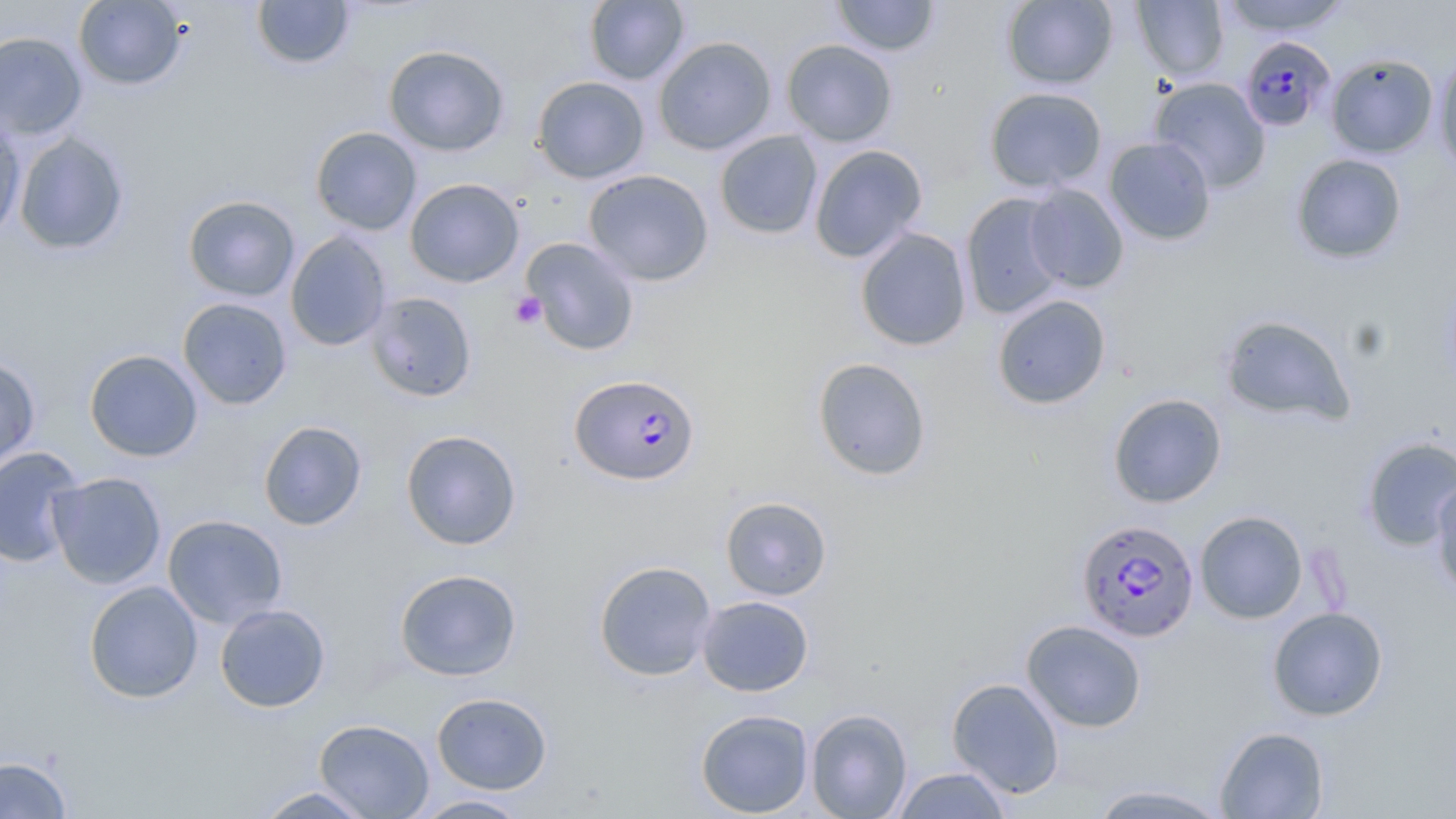

Summary:
  - Coordinate format: approximate bounding boxes as (x1, y1, x2, y2) in pixels
  - Uninfected red blood cell locations: (73, 0, 186, 91), (251, 0, 355, 70), (584, 0, 690, 86), (831, 0, 940, 57), (1000, 0, 1118, 90), (1132, 0, 1229, 81), (1219, 0, 1351, 36), (0, 31, 87, 140), (653, 36, 777, 155), (781, 39, 898, 147), (383, 44, 510, 156), (1326, 53, 1439, 158), (1433, 54, 1456, 179), (531, 76, 649, 184), (1148, 77, 1271, 193), (983, 87, 1107, 193), (0, 112, 26, 244), (310, 126, 422, 235), (715, 130, 823, 239), (13, 132, 130, 256), (1104, 137, 1216, 246), (809, 144, 927, 263), (1290, 153, 1407, 264), (583, 169, 714, 286), (405, 178, 524, 287), (1024, 184, 1130, 293), (959, 192, 1070, 320), (183, 194, 300, 302), (855, 227, 973, 352), (285, 231, 392, 351), (521, 237, 640, 356), (1440, 269, 1456, 397), (366, 292, 477, 402), (992, 294, 1111, 410), (177, 297, 293, 410), (1219, 313, 1356, 427), (84, 349, 203, 462), (0, 356, 41, 471), (812, 357, 932, 480), (1108, 393, 1227, 508), (258, 420, 368, 531), (400, 430, 522, 550), (1360, 435, 1456, 551), (0, 446, 85, 567), (48, 471, 166, 589), (1430, 476, 1456, 602), (720, 496, 832, 600), (1194, 509, 1308, 624), (163, 514, 288, 629), (593, 560, 718, 681), (394, 568, 522, 681), (84, 580, 204, 704), (697, 595, 814, 697), (214, 603, 331, 712), (1267, 606, 1388, 721), (1021, 619, 1147, 732), (946, 677, 1065, 797), (431, 691, 552, 794), (805, 708, 913, 819), (695, 709, 814, 817), (314, 718, 434, 818), (1214, 725, 1329, 818), (0, 756, 72, 818), (891, 766, 1013, 818), (1086, 783, 1235, 818), (252, 786, 378, 818), (411, 794, 533, 818)
  - Platelet locations: (510, 292, 546, 329)
  - Plasmodium falciparum-infected red blood cell locations: (1239, 36, 1335, 132), (569, 374, 700, 485), (1076, 518, 1200, 642)
  - Slide-level diagnosis: Plasmodium falciparum
  - Field of view: single
  - Image size: 1456×819 pixels
  - Preparation: thin blood film
  - Magnification: 1000x
  - Modality: optical microscopy
  - Stain: May-Grünwald-Giemsa